Outline each Plasmodium vivax-infected red blood cell.
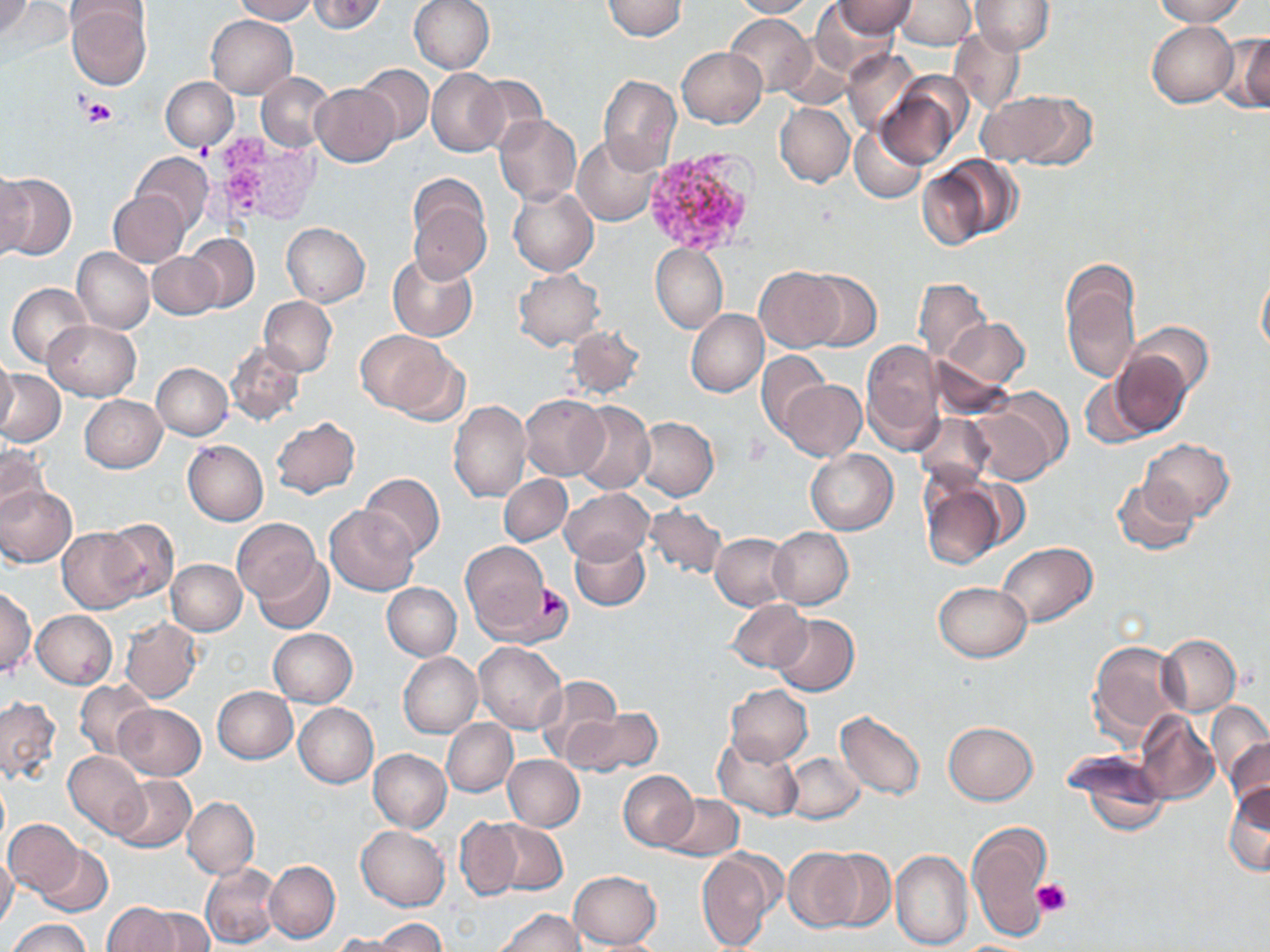
Approximate bounding boxes as (x1, y1, x2, y2) in pixels.
Plasmodium vivax-infected red blood cells: (640, 147, 759, 253).

slide-level diagnosis = Plasmodium vivax
stain = May-Grünwald-Giemsa
field of view = one of a larger specimen
uninfected red blood cell locations = approximate bounding boxes as (x1, y1, x2, y2) in pixels: (1, 0, 33, 39), (231, 0, 317, 23), (308, 0, 389, 34), (409, 0, 495, 74), (601, 0, 686, 41), (729, 0, 814, 18), (833, 0, 914, 36), (894, 0, 974, 51), (970, 0, 1053, 54), (1151, 0, 1247, 25), (810, 1, 898, 77), (65, 3, 152, 88), (960, 7, 1043, 92), (724, 13, 814, 96), (206, 15, 297, 97), (1146, 20, 1238, 107), (947, 26, 1026, 117), (1224, 32, 1270, 113), (675, 46, 766, 127), (842, 49, 919, 134), (355, 64, 433, 144), (427, 68, 506, 156), (256, 72, 334, 152), (597, 75, 681, 173), (469, 76, 547, 153), (161, 77, 238, 151), (875, 79, 964, 170), (311, 83, 397, 166), (979, 90, 1093, 168), (775, 102, 855, 187), (495, 114, 582, 207), (850, 125, 927, 204), (572, 135, 660, 226), (132, 152, 213, 232), (927, 157, 1022, 246), (0, 167, 31, 263), (0, 171, 76, 261), (407, 177, 493, 281), (507, 187, 598, 276), (107, 191, 190, 266), (281, 222, 370, 306), (186, 234, 260, 313), (651, 244, 728, 334), (73, 248, 154, 334), (149, 252, 222, 319), (387, 253, 478, 342), (1060, 265, 1140, 386), (1256, 266, 1270, 362), (756, 267, 843, 351), (513, 269, 605, 350), (804, 271, 881, 352), (913, 277, 992, 364), (7, 282, 93, 369), (258, 297, 337, 376), (685, 309, 767, 397), (940, 319, 1029, 389), (43, 321, 140, 401), (1123, 321, 1214, 398), (565, 325, 645, 400), (355, 330, 452, 416), (860, 341, 945, 454), (226, 342, 306, 425), (389, 348, 471, 425), (1106, 349, 1195, 440), (757, 351, 828, 436), (0, 354, 18, 439), (929, 354, 1017, 420), (153, 363, 233, 439), (0, 370, 66, 446), (1080, 374, 1160, 450), (779, 380, 866, 461), (519, 393, 610, 480), (79, 395, 167, 472), (967, 396, 1068, 485), (448, 399, 531, 501), (571, 401, 655, 495), (914, 411, 994, 489), (271, 416, 359, 499), (634, 417, 718, 501), (183, 439, 269, 525), (1141, 439, 1233, 522), (0, 443, 48, 521), (806, 449, 899, 535), (360, 474, 443, 558), (499, 475, 572, 546), (1112, 476, 1200, 556), (918, 477, 1006, 570), (0, 487, 76, 567), (560, 488, 652, 565), (643, 503, 727, 579), (325, 505, 419, 595), (97, 518, 180, 604), (231, 518, 322, 606), (58, 527, 144, 612), (769, 527, 853, 610), (711, 532, 793, 610), (570, 534, 650, 610), (997, 542, 1097, 626), (458, 543, 554, 638), (253, 553, 334, 634), (167, 560, 246, 635), (391, 582, 470, 735), (934, 582, 1030, 662), (382, 583, 461, 660), (0, 587, 36, 677), (726, 600, 811, 674), (32, 610, 117, 688), (771, 614, 859, 696), (121, 616, 202, 702), (268, 628, 358, 708), (1156, 634, 1241, 716), (1088, 640, 1186, 743), (399, 652, 482, 737), (535, 674, 624, 766), (75, 678, 157, 759), (725, 684, 812, 765), (213, 687, 298, 764), (0, 695, 60, 782), (1206, 700, 1269, 786), (294, 702, 378, 787), (115, 704, 206, 780), (574, 707, 662, 780), (835, 710, 926, 800), (1134, 712, 1219, 804), (441, 719, 517, 796), (943, 720, 1038, 804), (1222, 731, 1269, 819), (713, 736, 804, 821), (369, 749, 451, 832), (1066, 749, 1171, 834), (63, 751, 148, 838), (783, 753, 865, 824), (503, 755, 584, 830), (619, 770, 698, 850), (112, 776, 195, 852), (1223, 781, 1270, 876), (659, 793, 743, 859), (182, 797, 259, 879), (456, 818, 524, 899), (4, 820, 82, 896), (486, 820, 566, 895), (966, 821, 1053, 942), (356, 826, 448, 911), (36, 846, 113, 917), (783, 848, 861, 932), (818, 848, 895, 931), (695, 849, 780, 952), (890, 850, 972, 951), (0, 855, 19, 932), (265, 860, 340, 943), (201, 862, 282, 950), (568, 870, 661, 950), (101, 902, 187, 951), (135, 907, 212, 951), (495, 909, 584, 951), (6, 918, 91, 952), (374, 919, 447, 950), (329, 933, 406, 952)
preparation = thin blood film
platelet locations = approximate bounding boxes as (x1, y1, x2, y2) in pixels: (81, 96, 117, 128), (196, 140, 213, 163), (745, 434, 772, 463), (535, 583, 566, 619), (1033, 877, 1073, 917)
image size = 1270×952 pixels
magnification = 1000x
modality = light microscopy